Identify the blood parasite species.
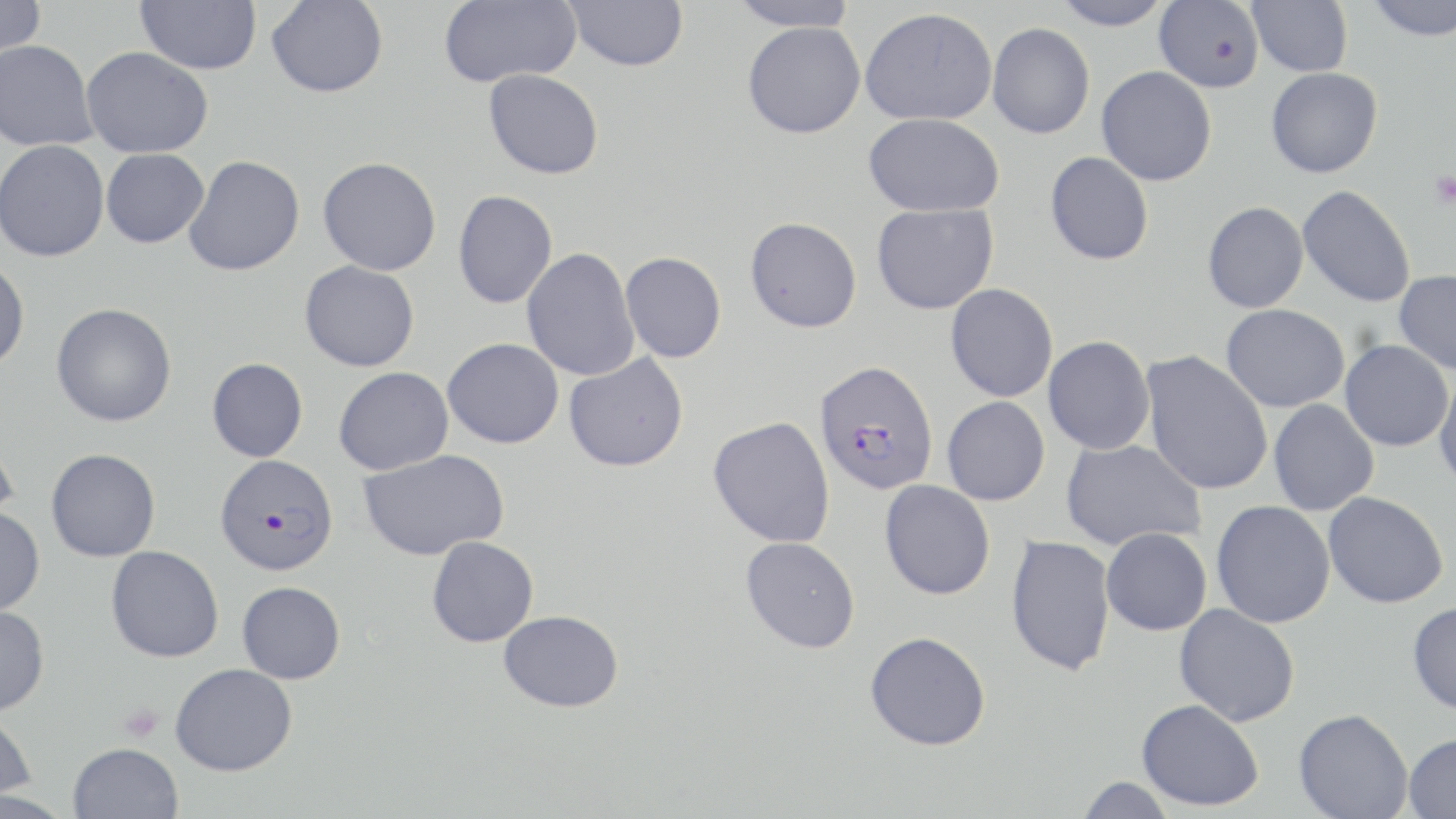
Plasmodium falciparum.

Approximate bounding boxes as (x1,y1)-(x2,y2) corner pairs in pixels. Platelet locations: (1430,171)-(1456,208), (118,704)-(164,742). Uninfected red blood cell locations: (0,0)-(46,60), (135,0)-(261,74), (266,0)-(389,98), (438,0)-(581,87), (564,0)-(688,72), (726,0)-(860,31), (1050,0)-(1174,30), (1154,0)-(1263,92), (1247,0)-(1352,76), (1365,0)-(1455,41), (860,7)-(998,126), (743,20)-(865,138), (987,22)-(1095,138), (0,40)-(99,151), (81,46)-(213,158), (1096,66)-(1217,186), (1266,67)-(1382,178), (483,69)-(604,179), (863,113)-(1005,217), (0,140)-(109,262), (101,148)-(209,248), (1044,151)-(1153,265), (184,155)-(305,276), (317,156)-(441,276), (1297,185)-(1416,307), (452,190)-(558,309), (1202,201)-(1309,313), (872,203)-(999,314), (745,216)-(862,333), (522,247)-(640,381), (620,251)-(726,363), (0,258)-(30,373), (299,260)-(419,372), (1394,270)-(1456,375), (945,284)-(1058,402), (51,303)-(177,427), (1221,304)-(1349,412), (1043,336)-(1155,455), (442,337)-(564,449), (1340,340)-(1453,451), (1141,351)-(1274,496), (563,352)-(689,472), (206,357)-(308,462), (333,367)-(453,475), (1433,369)-(1456,495), (942,396)-(1050,505), (1268,399)-(1379,516), (708,416)-(835,549), (0,432)-(19,527), (1061,438)-(1206,551), (46,448)-(160,562), (357,449)-(510,561), (879,480)-(995,600), (1323,491)-(1448,608), (1212,500)-(1336,628), (0,507)-(45,615), (1101,527)-(1212,636), (1005,534)-(1116,677), (427,536)-(539,647), (740,536)-(861,653), (106,545)-(224,662), (237,581)-(346,684), (1407,601)-(1456,716), (1174,603)-(1301,727), (0,605)-(49,715), (498,610)-(624,712), (864,631)-(991,751), (170,663)-(297,776), (1136,699)-(1264,811), (1293,708)-(1412,819), (0,712)-(37,801), (1403,732)-(1456,819), (68,742)-(183,819), (1074,777)-(1177,818). Plasmodium falciparum-infected red blood cell locations: (815,360)-(938,495), (215,454)-(338,575). Thin blood smear. Captured at 1000x magnification. One field of a larger specimen. Optical microscopy. Image is 1456×819 pixels. May-Grünwald-Giemsa stain.